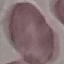
Result: negative for malaria parasites. Thin smear of blood. Cell patch, automatically extracted from a larger field of view and resized to 64 × 64 pixels. Acquired by smartphone through the microscope eyepiece. Giemsa-stained preparation.